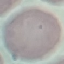

Summary:
  - Malaria status: uninfected
  - Preparation: thin smear
  - Stain: Giemsa
  - Capture: smartphone camera at the microscope eyepiece
  - Image type: cell patch, automatically extracted from a larger field of view and resized to 64 × 64 pixels